Classify this cell by malaria status.
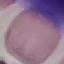

It is uninfected.

Summary:
  - Image type: automatically extracted cell patch, resized to 64 × 64 pixels
  - Capture: smartphone through the microscope eyepiece
  - Stain: Giemsa
  - Preparation: thin smear